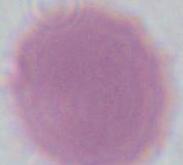

Summary:
  - Magnification: 1000x
  - Identification: red blood cell
  - Modality: micrograph